Give the position of every Plasmodium parasite.
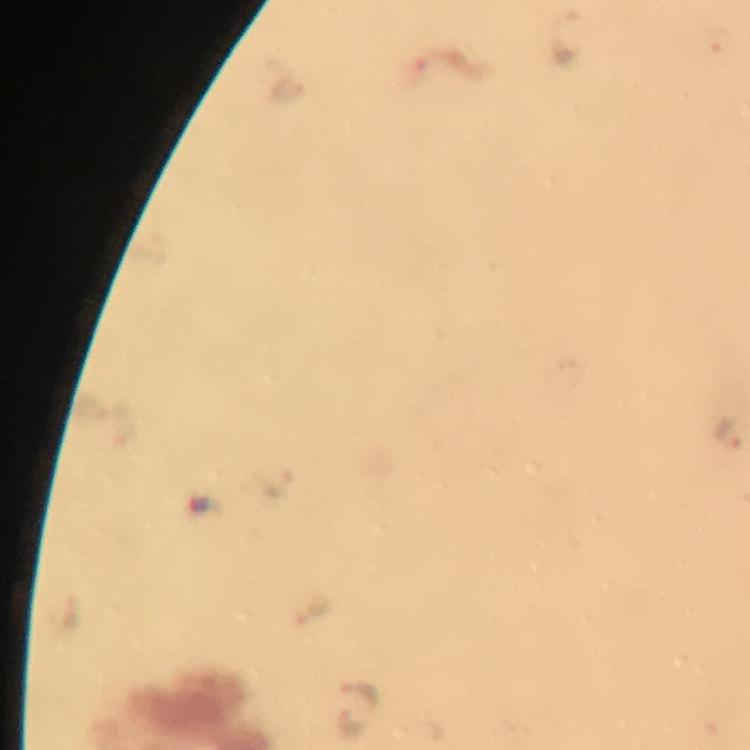

Approximate object centers, in pixels from the top-left corner.
Plasmodium parasites: (x=727, y=431), (x=315, y=611), (x=361, y=691), (x=353, y=724).

Summary:
  - Context: from a malaria diagnostic workup
  - Magnification: 100x
  - Capture: smartphone mounted on the microscope
  - Preparation: thick smear
  - Image size: 750×750 pixels
  - Immersion oil: applied
  - Cropped from: one field of view
  - Stain: Giemsa